Point out each leukocyte.
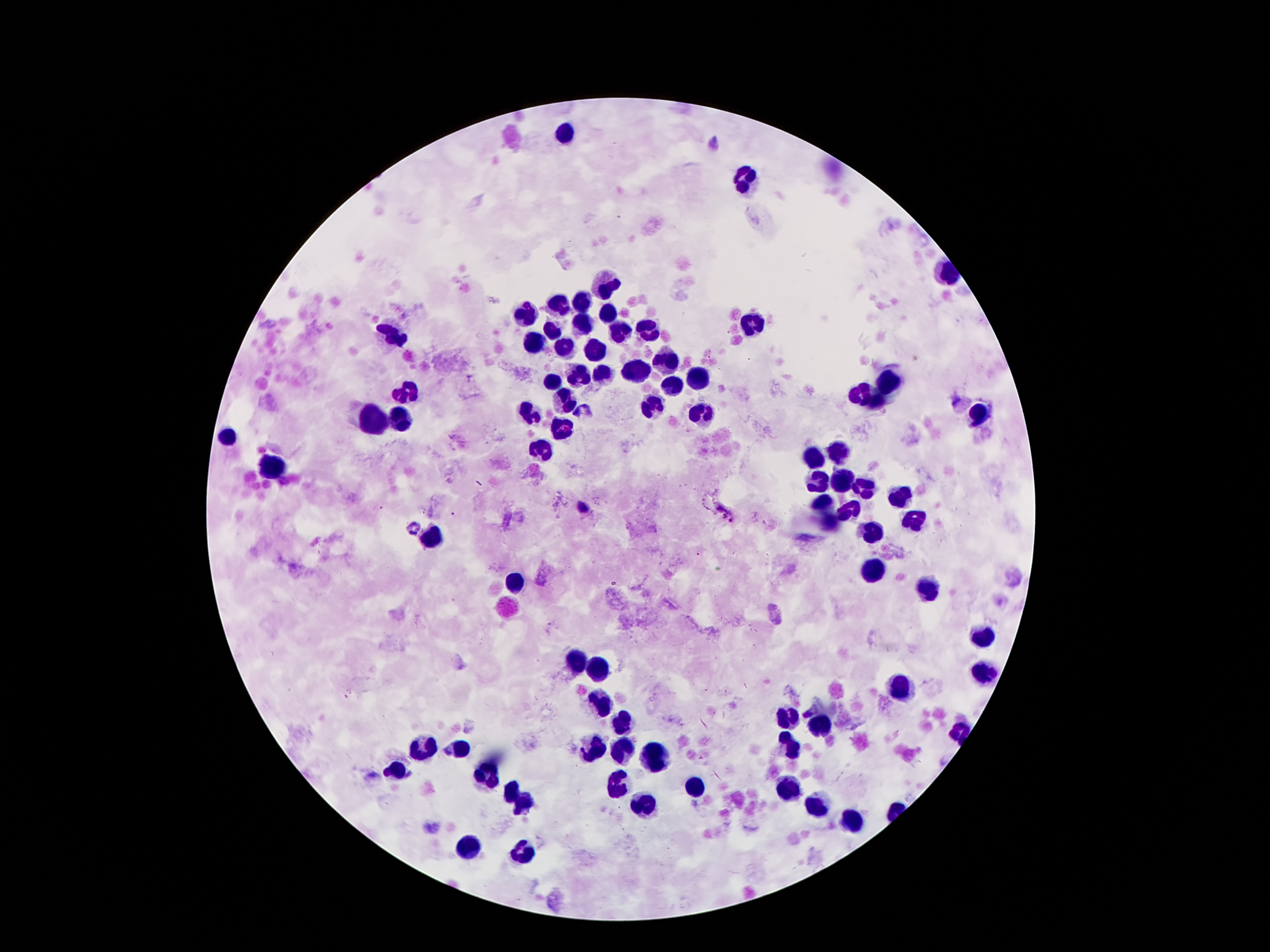

Approximate centers as {x, y} in pixels.
Leukocytes: {564, 135}, {745, 178}, {607, 286}, {583, 302}, {558, 305}, {526, 312}, {607, 317}, {583, 324}, {752, 327}, {552, 331}, {646, 331}, {617, 334}, {394, 336}, {533, 343}, {567, 346}, {598, 349}, {667, 362}, {634, 372}, {581, 375}, {605, 375}, {697, 377}, {555, 382}, {888, 386}, {673, 389}, {855, 392}, {408, 393}, {565, 398}, {653, 404}, {876, 405}, {531, 411}, {703, 413}, {977, 416}, {399, 418}, {377, 425}, {562, 430}, {229, 438}, {540, 449}, {840, 451}, {812, 459}, {274, 468}, {840, 480}, {816, 482}, {866, 490}, {902, 495}, {826, 504}, {852, 509}, {831, 519}, {915, 519}, {867, 531}, {428, 539}, {874, 572}, {514, 582}, {929, 589}, {982, 640}, {574, 661}, {598, 670}, {980, 674}, {902, 688}, {603, 703}, {788, 717}, {620, 727}, {818, 729}, {595, 747}, {421, 749}, {620, 749}, {464, 750}, {790, 750}, {658, 757}, {396, 770}, {490, 777}, {619, 788}, {694, 791}, {785, 791}, {511, 795}, {818, 803}, {637, 804}, {524, 805}, {847, 819}, {468, 850}, {524, 855}.

Summary:
  - Malaria parasite locations: {582, 506}
  - Field of view: one from this slide
  - Capture: smartphone camera through the microscope eyepiece
  - Patient malaria status: infected with Plasmodium falciparum
  - Magnification: 100x
  - Stain: Giemsa
  - Image size: 1270×952 pixels
  - Preparation: thick blood film